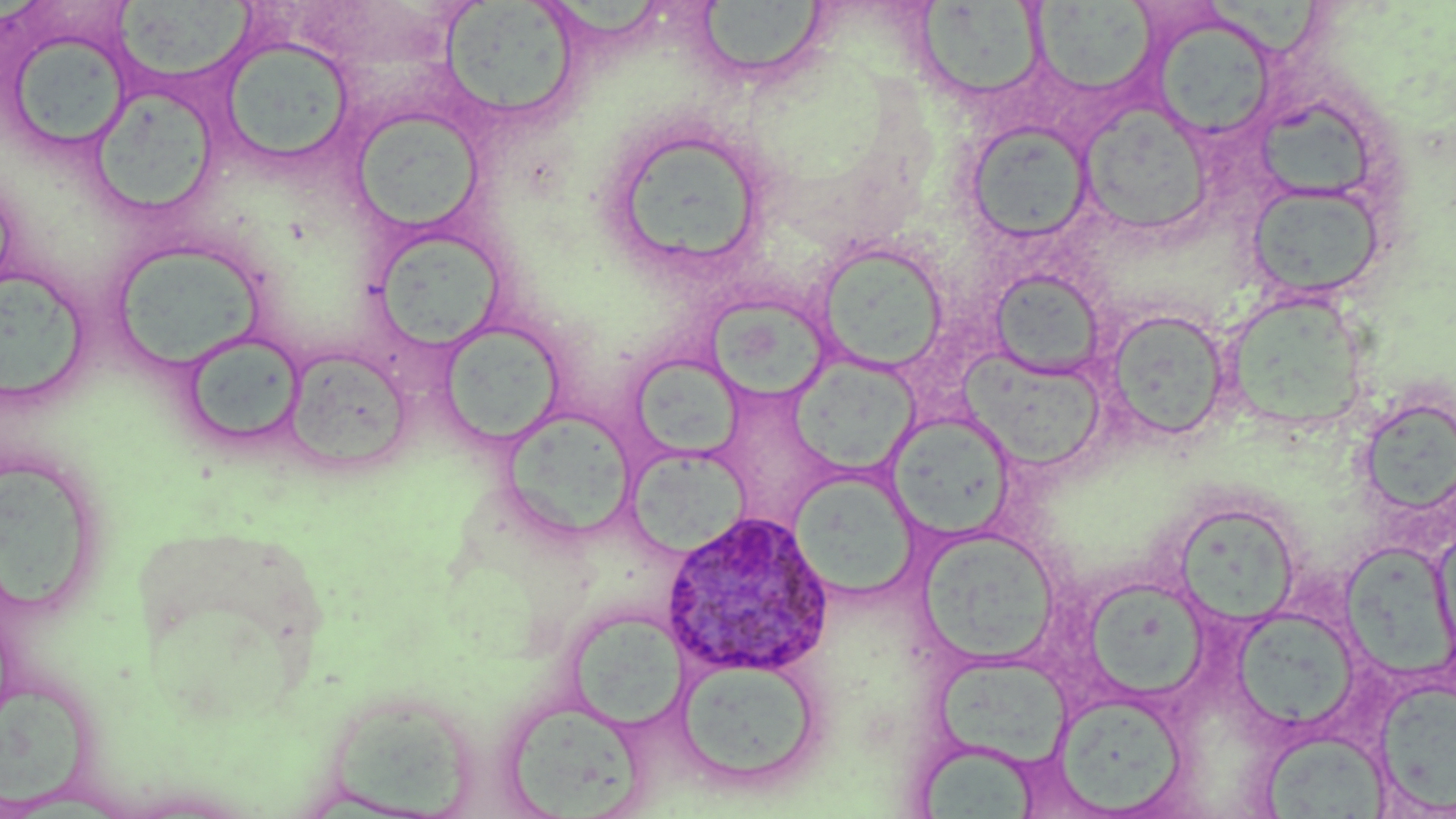

slide-level diagnosis = Plasmodium ovale
preparation = thin blood smear
uninfected red blood cell locations = approximate bounding boxes as (x1,y1)-(x2,y2) corner pairs in pixels: (702,0)-(830,78), (441,1)-(579,124), (1031,2)-(1156,94), (115,3)-(255,82), (915,3)-(1047,100), (1148,11)-(1279,142), (4,25)-(133,156), (218,37)-(356,168), (96,92)-(217,212), (1079,103)-(1213,236), (1262,106)-(1378,204), (351,108)-(485,234), (965,121)-(1094,243), (602,122)-(773,279), (0,167)-(19,302), (1246,181)-(1387,300), (370,228)-(506,352), (815,241)-(950,375), (112,242)-(266,371), (0,269)-(88,404), (989,269)-(1106,378), (706,295)-(832,401), (1228,298)-(1366,434), (1104,308)-(1231,441), (438,321)-(565,446), (183,331)-(306,448), (284,345)-(412,472), (959,354)-(1107,475), (629,355)-(745,458), (789,356)-(920,477), (1358,394)-(1456,522), (501,408)-(639,541), (887,413)-(1017,539), (623,447)-(751,558), (1,462)-(92,613), (790,471)-(920,599), (1171,500)-(1302,627), (916,526)-(1062,667), (1432,527)-(1456,666), (1091,582)-(1207,702), (1232,606)-(1360,732), (566,607)-(689,733), (677,657)-(822,789), (936,660)-(1082,772), (1375,679)-(1456,814), (0,686)-(99,810), (1054,691)-(1190,815), (502,698)-(649,816), (334,702)-(469,819), (1259,731)-(1390,817), (916,749)-(1040,819)
magnification = 1000x
field of view = single
image size = 1456×819 pixels
modality = light microscopy
stain = May-Grünwald-Giemsa
Plasmodium ovale-infected red blood cell locations = approximate bounding boxes as (x1,y1)-(x2,y2) corner pairs in pixels: (661,509)-(835,678)